Report the malaria status of this cell.
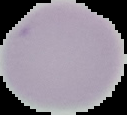

Uninfected.

The area outside the segmented cell region is set to black. Image is 127×115 pixels. From a thin blood smear.